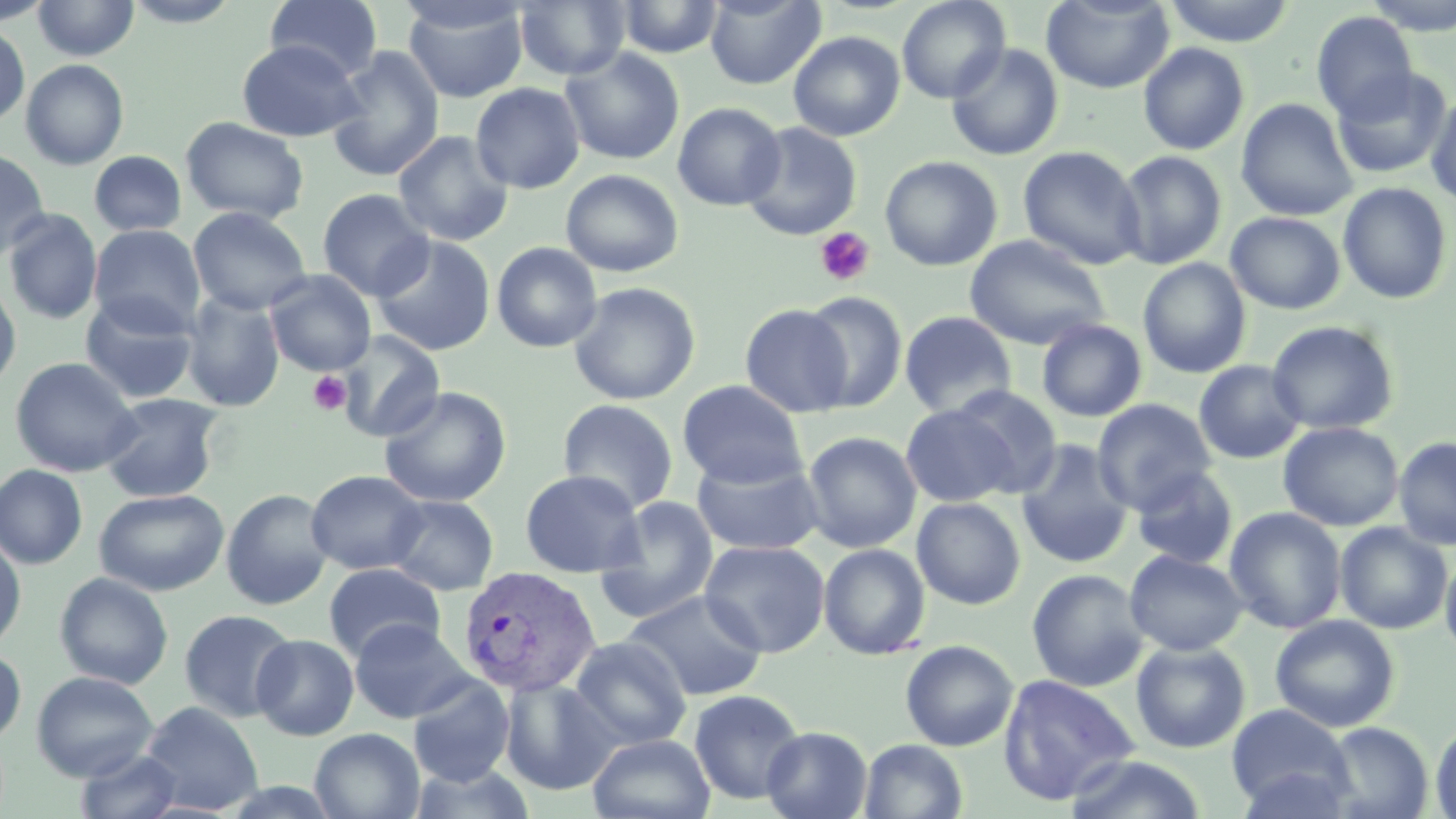
Summary:
  - Coordinate format: approximate bounding boxes as (x1,y1)-(x2,y2) corner pairs in pixels
  - Uninfected red blood cell locations: (0,0)-(54,26), (32,0)-(140,60), (122,0)-(243,28), (265,0)-(384,81), (514,0)-(630,81), (612,0)-(725,59), (705,0)-(826,89), (896,0)-(1011,104), (1041,0)-(1175,93), (1162,0)-(1295,47), (1362,0)-(1456,36), (401,2)-(530,102), (1311,11)-(1418,121), (0,24)-(30,126), (788,31)-(905,141), (236,40)-(365,142), (945,42)-(1064,161), (1138,42)-(1250,155), (324,46)-(445,183), (558,47)-(685,165), (20,59)-(129,170), (1331,65)-(1453,179), (470,82)-(585,194), (1425,90)-(1456,209), (1235,98)-(1358,221), (671,102)-(786,211), (180,117)-(309,225), (740,121)-(863,241), (393,130)-(514,246), (1018,145)-(1146,271), (0,150)-(50,259), (89,150)-(187,236), (1115,150)-(1227,270), (880,155)-(1003,271), (560,168)-(684,277), (1337,183)-(1454,305), (317,188)-(435,301), (188,206)-(311,315), (3,209)-(103,325), (1226,211)-(1346,314), (89,224)-(205,334), (371,235)-(496,356), (964,235)-(1110,350), (491,241)-(603,353), (1137,258)-(1251,378), (265,270)-(376,376), (0,277)-(22,394), (567,281)-(701,405), (801,291)-(908,412), (80,293)-(200,404), (180,293)-(285,413), (740,304)-(853,417), (899,310)-(1018,419), (1036,318)-(1147,422), (1266,321)-(1399,435), (334,331)-(445,443), (10,357)-(141,477), (1193,360)-(1306,464), (677,380)-(808,488), (946,385)-(1063,496), (378,386)-(512,508), (99,392)-(224,503), (1092,398)-(1217,514), (557,399)-(679,514), (899,403)-(1020,508), (1278,422)-(1404,532), (802,431)-(922,553), (1393,435)-(1456,552), (1015,440)-(1135,569), (691,453)-(825,555), (0,464)-(88,569), (1131,466)-(1239,570), (305,469)-(429,575), (519,469)-(646,577), (221,488)-(333,610), (94,489)-(229,596), (593,494)-(720,625), (384,495)-(499,595), (912,497)-(1026,610), (1224,507)-(1347,634), (1334,521)-(1454,635), (0,534)-(26,652), (699,539)-(830,658), (818,543)-(931,660), (1439,549)-(1456,663), (1125,550)-(1248,656), (323,562)-(446,662), (1026,568)-(1149,692), (54,572)-(174,689), (623,589)-(768,701), (179,609)-(299,723), (1270,615)-(1400,733), (349,617)-(474,724), (251,634)-(359,740), (569,636)-(691,750), (900,640)-(1019,751), (1130,641)-(1250,753), (0,647)-(27,745), (31,671)-(158,782), (997,673)-(1140,805), (407,675)-(514,788), (499,677)-(621,796), (688,689)-(807,805), (139,701)-(263,815), (1227,703)-(1353,815), (1430,720)-(1456,818), (1321,721)-(1434,818), (762,726)-(872,819), (310,728)-(425,819), (586,733)-(716,819), (858,739)-(968,819), (74,747)-(185,819), (1061,754)-(1211,818)
  - Platelet locations: (814,227)-(876,287), (308,370)-(352,415)
  - Plasmodium vivax-infected red blood cell locations: (456,565)-(601,699)
  - Slide-level diagnosis: Plasmodium vivax
  - Preparation: thin blood film
  - Field of view: one of a larger specimen
  - Stain: May-Grünwald-Giemsa
  - Magnification: 1000x
  - Modality: optical microscopy
  - Image size: 1456×819 pixels